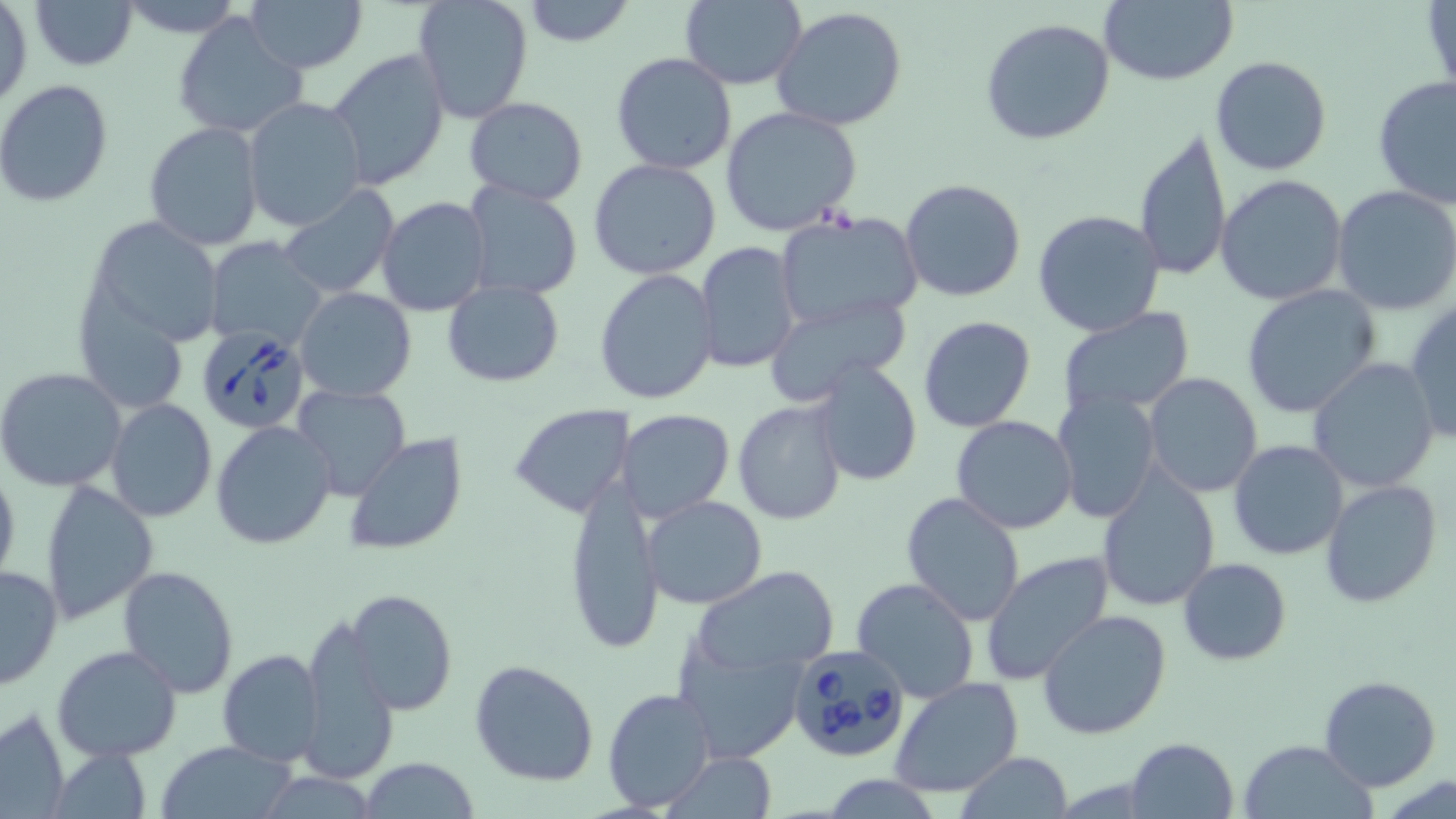
slide-level diagnosis = Babesia divergens
modality = optical microscopy
image size = 1456×819 pixels
Babesia divergens-infected red blood cell locations = approximate bounding boxes as (x1, y1, x2, y2) in pixels: (193, 326, 312, 435), (787, 644, 912, 763)
magnification = 1000x
field of view = single
preparation = thin blood film
stain = May-Grünwald-Giemsa
uninfected red blood cell locations = approximate bounding boxes as (x1, y1, x2, y2) in pixels: (29, 0, 139, 70), (116, 0, 246, 39), (245, 0, 366, 73), (411, 0, 535, 124), (523, 0, 633, 47), (1102, 0, 1240, 86), (678, 1, 808, 89), (1, 3, 33, 111), (771, 7, 910, 132), (172, 12, 307, 140), (978, 17, 1118, 146), (326, 49, 452, 192), (611, 51, 739, 175), (1208, 55, 1332, 176), (1373, 76, 1456, 207), (0, 80, 117, 208), (241, 96, 368, 232), (464, 96, 589, 203), (720, 107, 861, 235), (144, 120, 267, 252), (1134, 129, 1232, 282), (588, 159, 722, 281), (1215, 174, 1348, 305), (899, 177, 1028, 304), (461, 180, 584, 302), (1332, 186, 1456, 316), (277, 188, 399, 297), (376, 196, 491, 318), (1032, 209, 1166, 336), (88, 215, 222, 347), (773, 216, 924, 331), (203, 237, 329, 348), (696, 242, 802, 374), (594, 269, 719, 405), (443, 280, 563, 386), (77, 285, 189, 412), (1241, 285, 1381, 419), (295, 287, 417, 401), (765, 291, 915, 402), (1404, 301, 1456, 446), (1056, 308, 1197, 422), (918, 315, 1036, 434), (1307, 357, 1441, 492), (812, 359, 924, 486), (0, 368, 129, 493), (1142, 373, 1263, 499), (293, 384, 411, 501), (1053, 392, 1161, 524), (732, 395, 849, 524), (106, 398, 218, 521), (509, 403, 633, 518), (619, 409, 735, 523), (950, 414, 1077, 535), (211, 419, 337, 549), (344, 433, 469, 555), (1229, 439, 1350, 561), (0, 463, 20, 591), (1093, 469, 1220, 612), (565, 474, 666, 658), (1319, 479, 1442, 610), (40, 481, 158, 625), (901, 491, 1026, 625), (642, 495, 768, 608), (980, 550, 1115, 685), (1178, 558, 1291, 664), (0, 563, 63, 689), (117, 565, 239, 698), (695, 569, 845, 668), (851, 577, 979, 702), (350, 588, 456, 715), (1038, 607, 1172, 739), (296, 614, 398, 786), (674, 639, 810, 765), (52, 644, 184, 763), (217, 650, 326, 766), (469, 660, 599, 787), (1317, 676, 1442, 792), (890, 677, 1024, 799), (603, 685, 715, 811), (1, 707, 70, 818), (1125, 737, 1240, 819), (1238, 739, 1377, 819), (155, 741, 300, 819), (671, 752, 778, 819), (955, 752, 1073, 818), (361, 757, 479, 818)